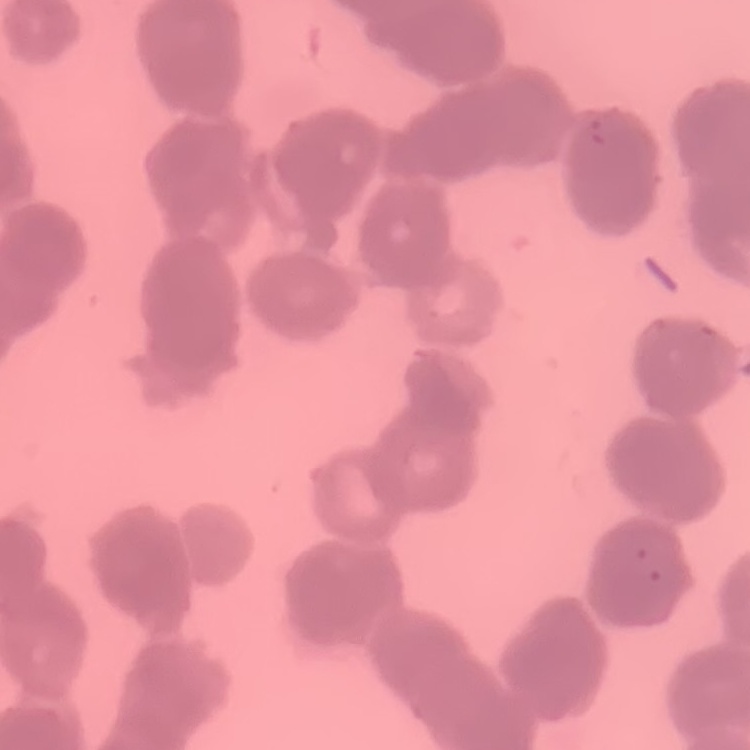
Summary:
  - Erythrocyte morphology: rouleaux formation
  - Image type: one tile cut from a larger photomicrograph
  - Stain: Field's or Giemsa
  - Preparation: thin blood smear